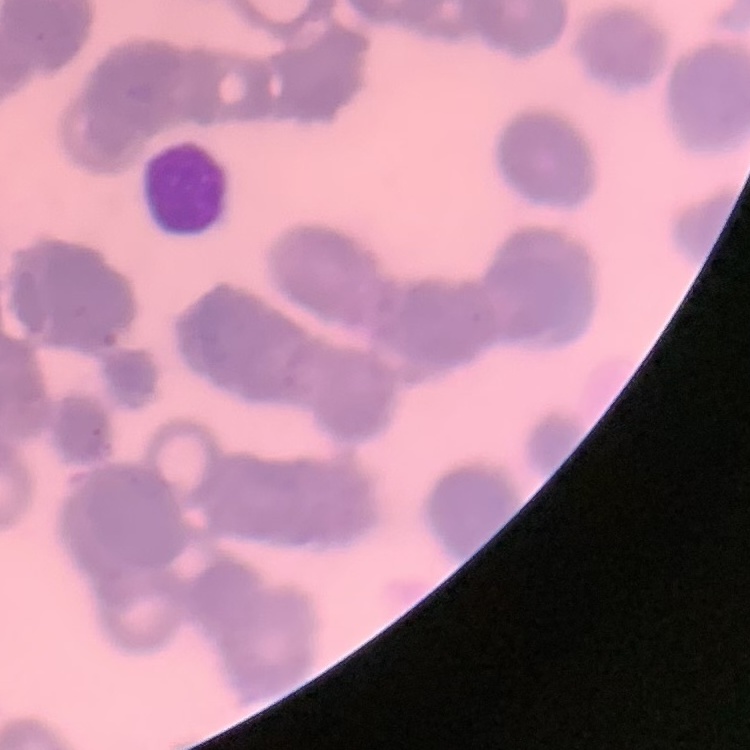 The red blood cells show rouleaux formation. Field's or Giemsa stain. Thin peripheral smear. Square crop of a larger photomicrograph.